Point out each malaria parasite and each leukocyte.
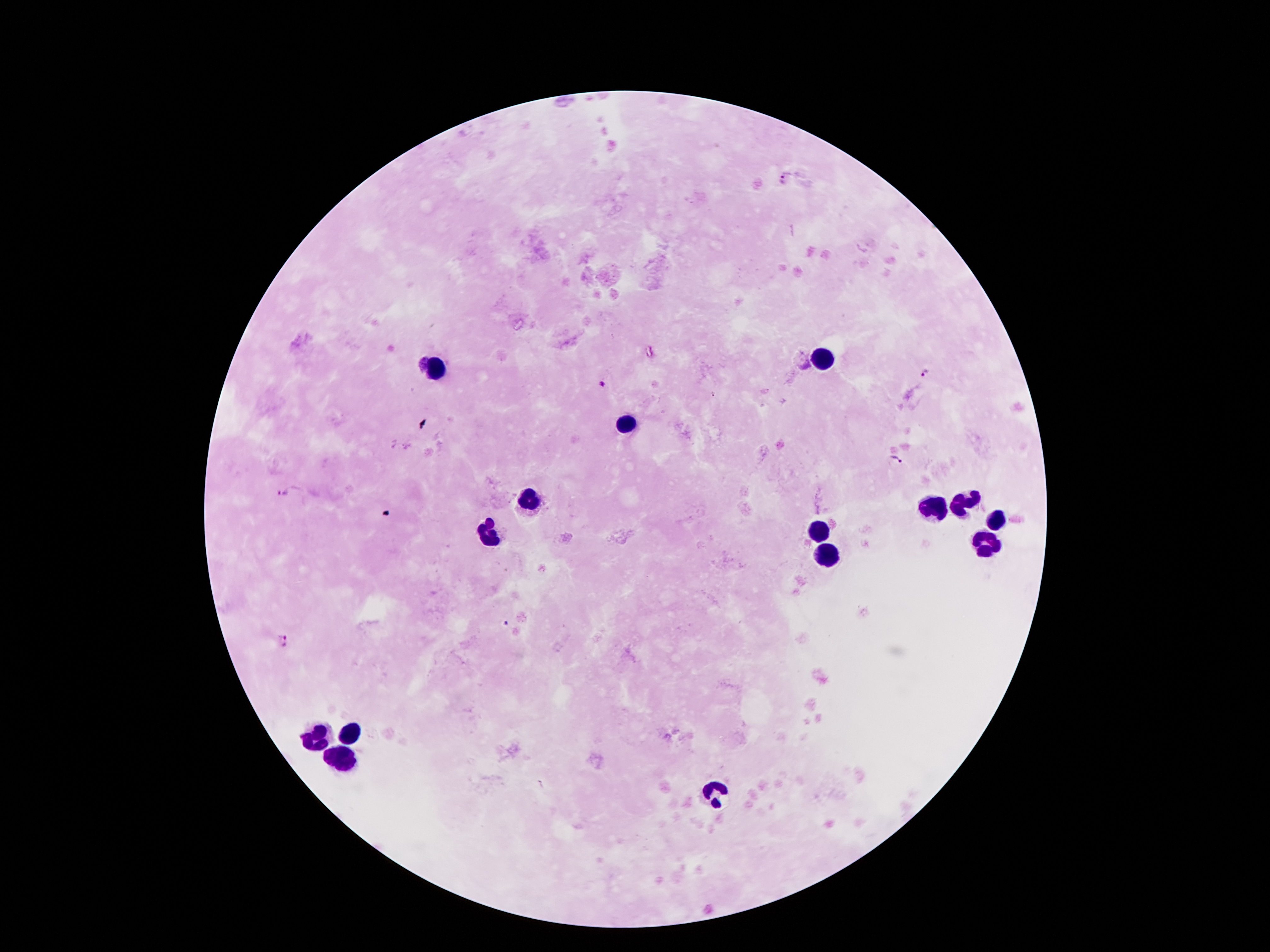
Approximate centers as (x, y) in pixels.
Malaria parasites: (783, 181), (925, 377), (598, 383), (897, 458), (284, 492), (284, 642).
Leukocytes: (822, 360), (432, 369), (631, 422), (527, 496), (963, 499), (929, 508), (994, 519), (820, 532), (491, 533), (990, 546), (826, 555), (352, 732), (318, 737), (341, 762), (715, 793).

Summary:
  - Capture: smartphone camera through the microscope eyepiece
  - Preparation: thick blood smear
  - Image size: 1270×952 pixels
  - Field of view: single
  - Patient malaria status: infected with Plasmodium falciparum
  - Magnification: 100x
  - Stain: Giemsa